Assess this cell for malaria.
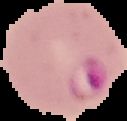
Parasitized.

From a thin blood film. Image is 127×121 pixels. Segmented cell region on a black background.